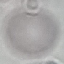

Result: no malaria parasites seen. Giemsa-stained preparation. Thin blood smear. Acquired by smartphone through the microscope eyepiece. Automatically extracted cell patch, resized to 64 × 64 pixels.